Identify the preparation type.
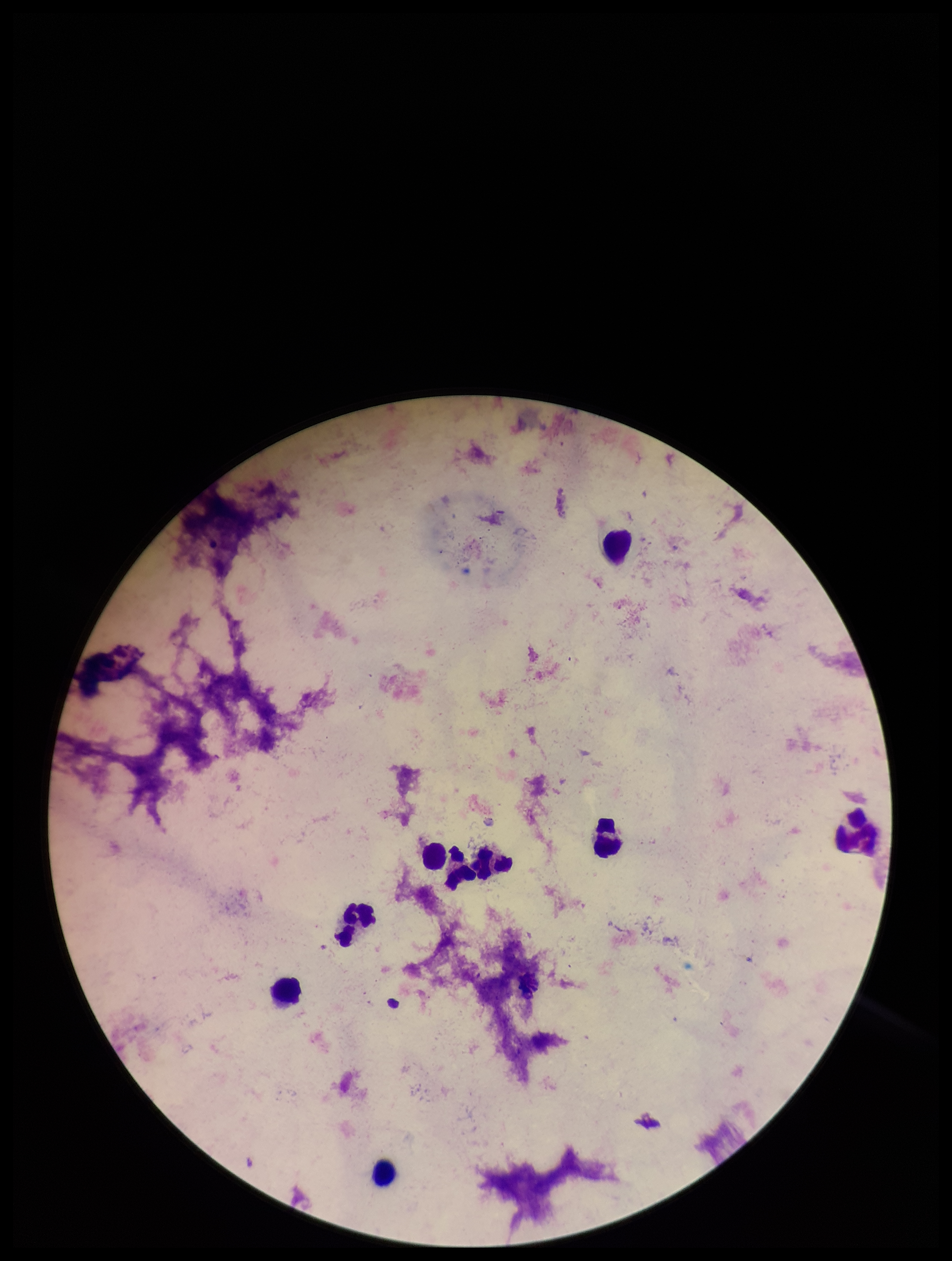

It is a thick blood smear.

Parasite count: 0. Leukocyte count: 9. Plasmodium parasites: none seen. Giemsa stain. Smartphone photograph taken through the eyepiece of a microscope. Patient malaria status: negative. Single field of view. Image is 952×1261 pixels.